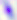

modality = photomicrograph
identification = Toxoplasma gondii
magnification = 400x